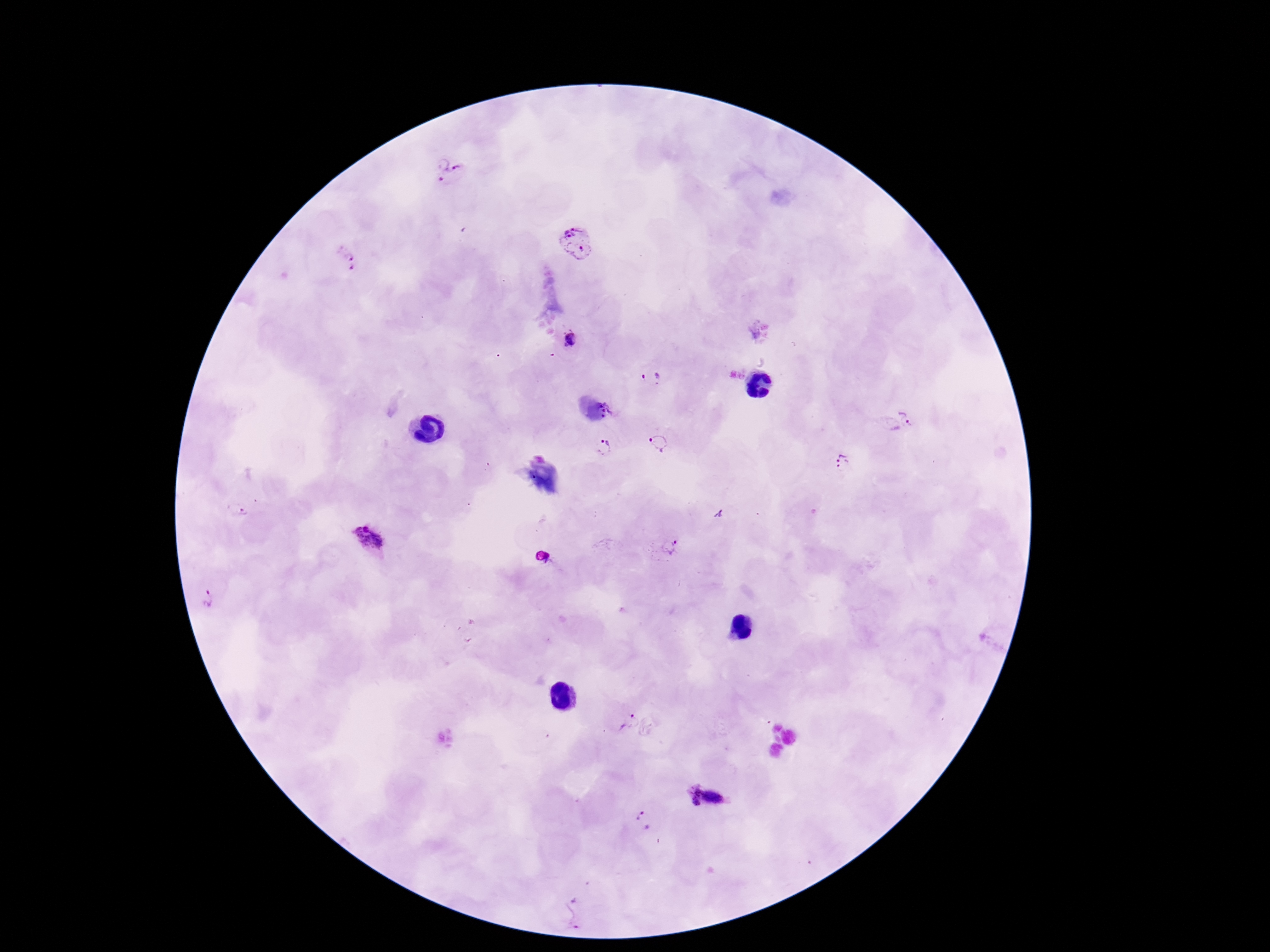
patient malaria status = infected
field of view = single
magnification = 100x
Plasmodium parasite locations = approximate centers as {x, y} in pixels: {452, 172}, {576, 242}, {346, 258}, {569, 339}, {651, 376}, {606, 408}, {910, 417}, {659, 443}, {601, 447}, {842, 461}, {240, 507}, {369, 538}, {669, 546}, {208, 598}, {631, 721}, {704, 797}, {644, 822}, {575, 914}
stain = Giemsa
capture = smartphone camera through the microscope eyepiece
image size = 1270×952 pixels
preparation = thick blood film